Report the malaria status of this cell.
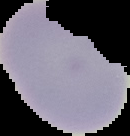
It is uninfected.

{
  "image_type": "cell region segmented out of the field of view; surrounding area masked to black",
  "image_size": "130×136 pixels",
  "preparation": "thin blood film"
}